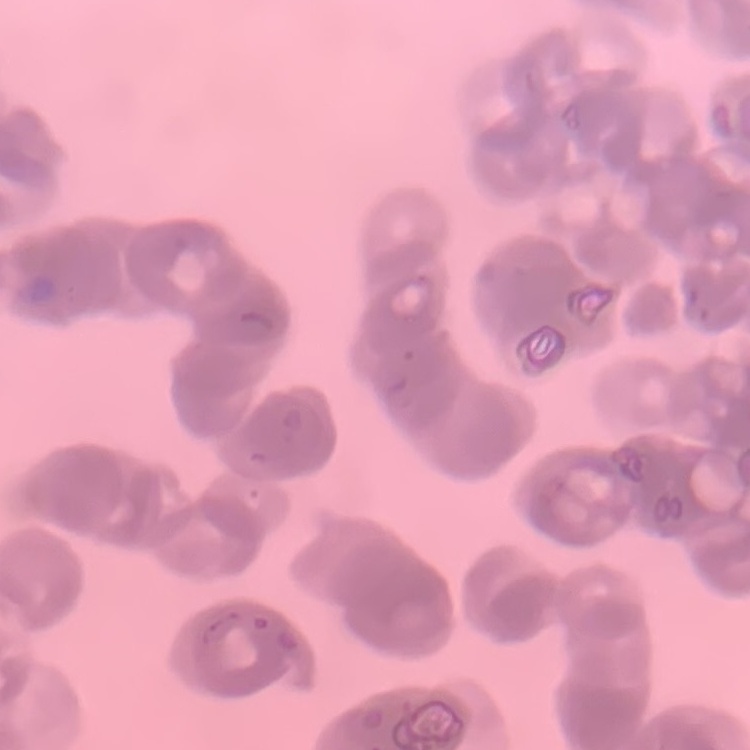

{
  "red_blood_cell_morphology": "rouleaux formation",
  "stain": "Field's or Giemsa",
  "preparation": "thin blood film",
  "image_type": "one tile cut from a larger photomicrograph"
}